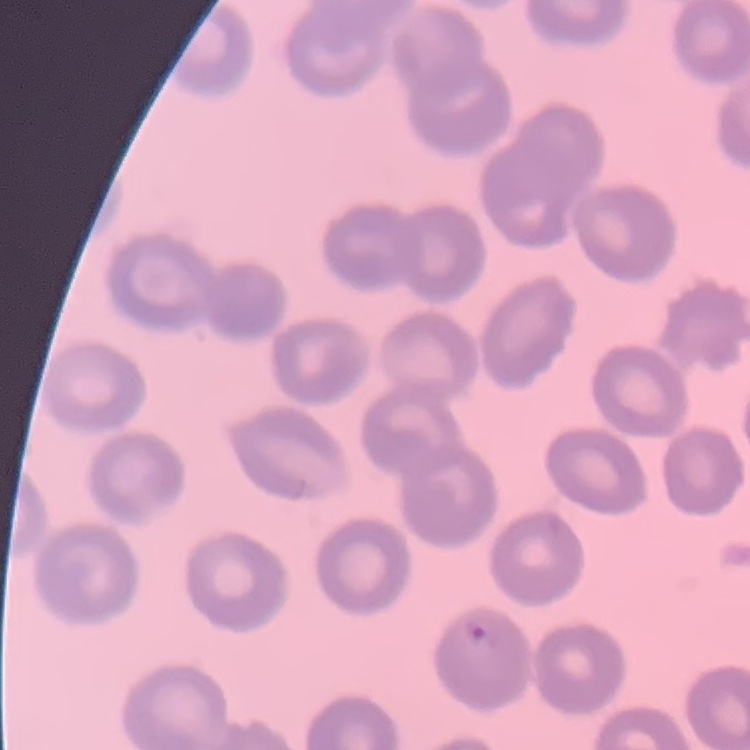

The erythrocytes exhibit no rouleaux formation. One tile cut from a larger photomicrograph. Thin blood film. Stained with either Field's or Giemsa.